Assess for malaria.
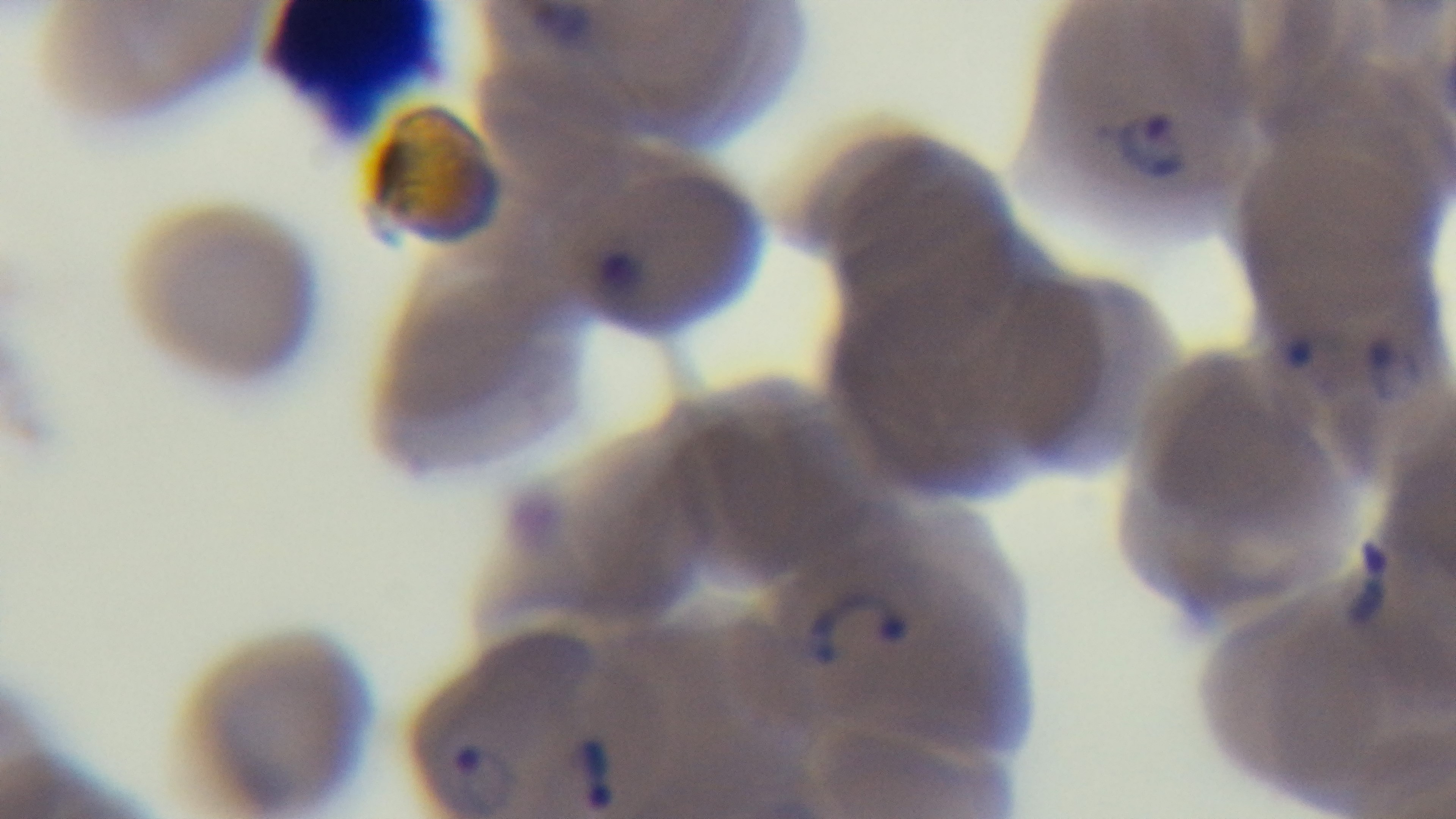
It is infected.

Summary:
  - Objective: 100x oil immersion
  - Field of view: single
  - Stain: Giemsa
  - Preparation: thin blood film
  - Capture: mounted 4K digital camera
  - Modality: light microscopy